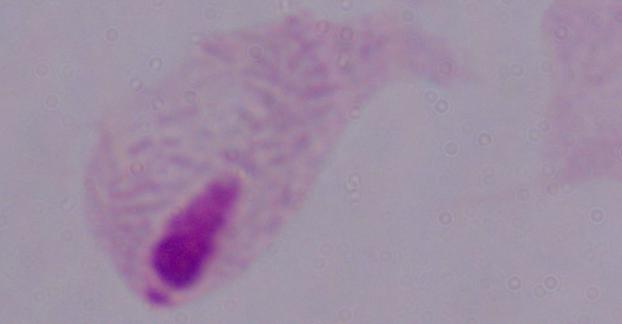 1000x magnification. A trichomonad is shown. Micrograph.